Classify this cell by malaria status.
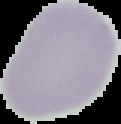
It is uninfected.

Summary:
  - Image type: segmented cell region on a black background
  - Preparation: thin blood smear
  - Image size: 121×124 pixels